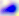

{
  "modality": "micrograph",
  "identification": "Toxoplasma gondii",
  "magnification": "400x"
}